Locate leukocytes (white blood cells).
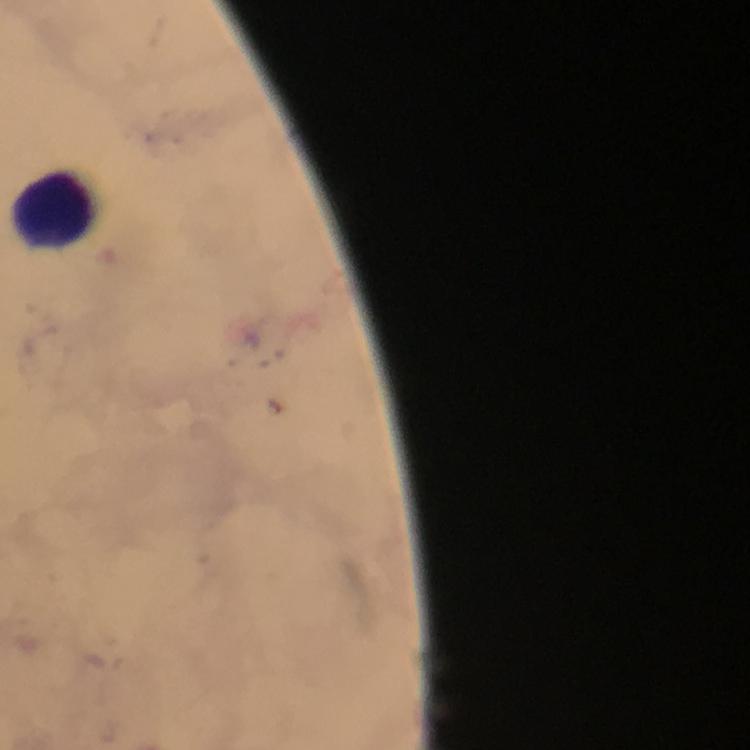
Approximate centers as [x, y] in pixels.
Leukocytes: [55, 212].

Plasmodium parasites: none detected. A crop from one field of view. Thick blood smear. Image is 750×750 pixels. Immersion oil was used. Giemsa stain. Photographed through the microscope with a smartphone camera. At 100x magnification. From a malaria diagnostic workup.